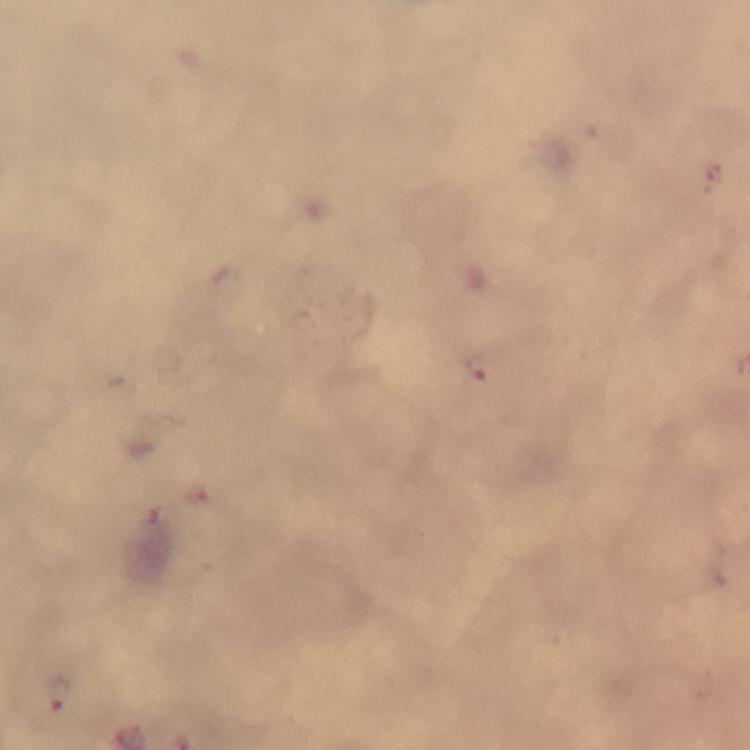

Approximate centers as [x, y] in pixels.
Summary:
  - Plasmodium parasite locations: [482, 370], [198, 494], [61, 694]
  - Stain: Giemsa
  - Preparation: thick smear
  - Image size: 750×750 pixels
  - Immersion oil: applied
  - Cropped from: a single field of view
  - Capture: smartphone mounted on the microscope
  - Magnification: 100x
  - Context: from a malaria diagnostic workup